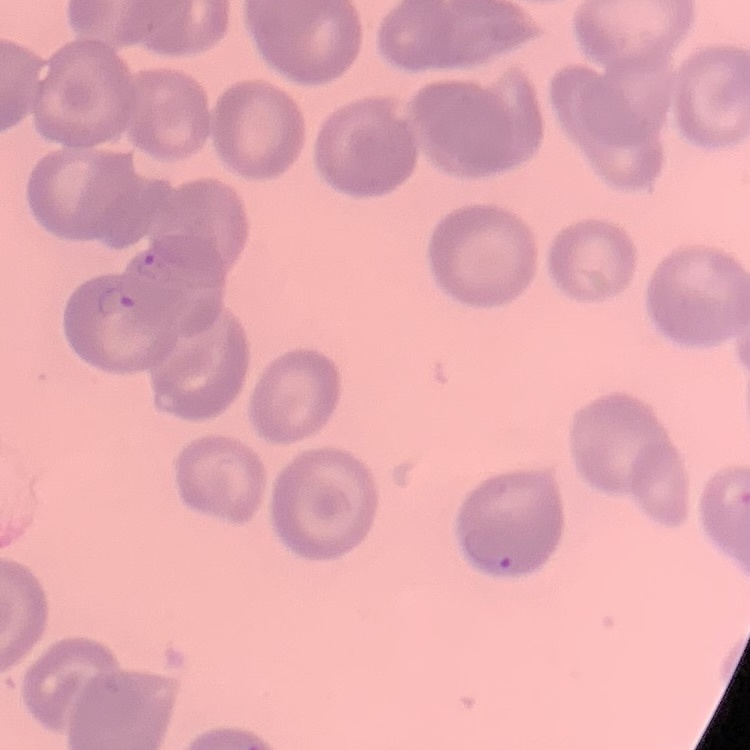
Summary:
  - Erythrocyte morphology: no rouleaux formation
  - Image type: square crop of a larger photomicrograph
  - Stain: Field's or Giemsa
  - Preparation: thin peripheral smear